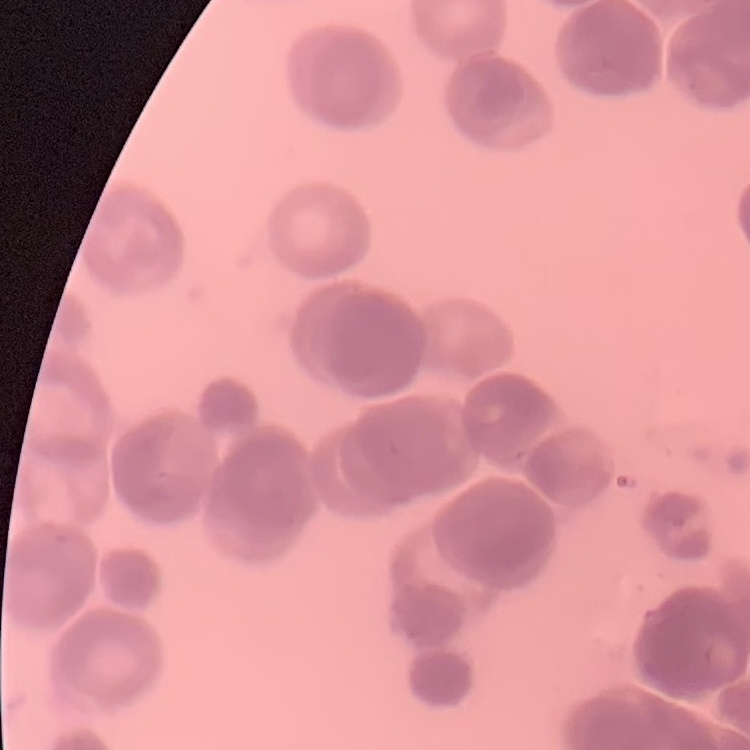 The erythrocytes exhibit rouleaux formation. Field's or Giemsa stain. One tile cut from a larger photomicrograph. Thin blood film.